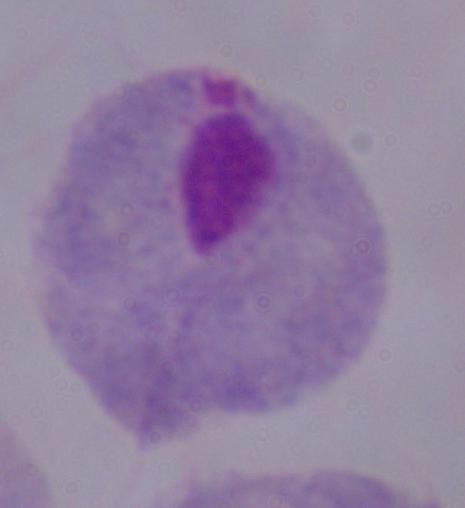
identification: trichomonad
magnification: 1000x
modality: micrograph